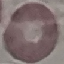
{
  "malaria_status": "uninfected",
  "capture": "smartphone through the microscope eyepiece",
  "preparation": "thin smear",
  "image_type": "cell patch, automatically extracted from a larger field of view and resized to 64 × 64 pixels",
  "stain": "Giemsa"
}